Look for Plasmodium parasites.
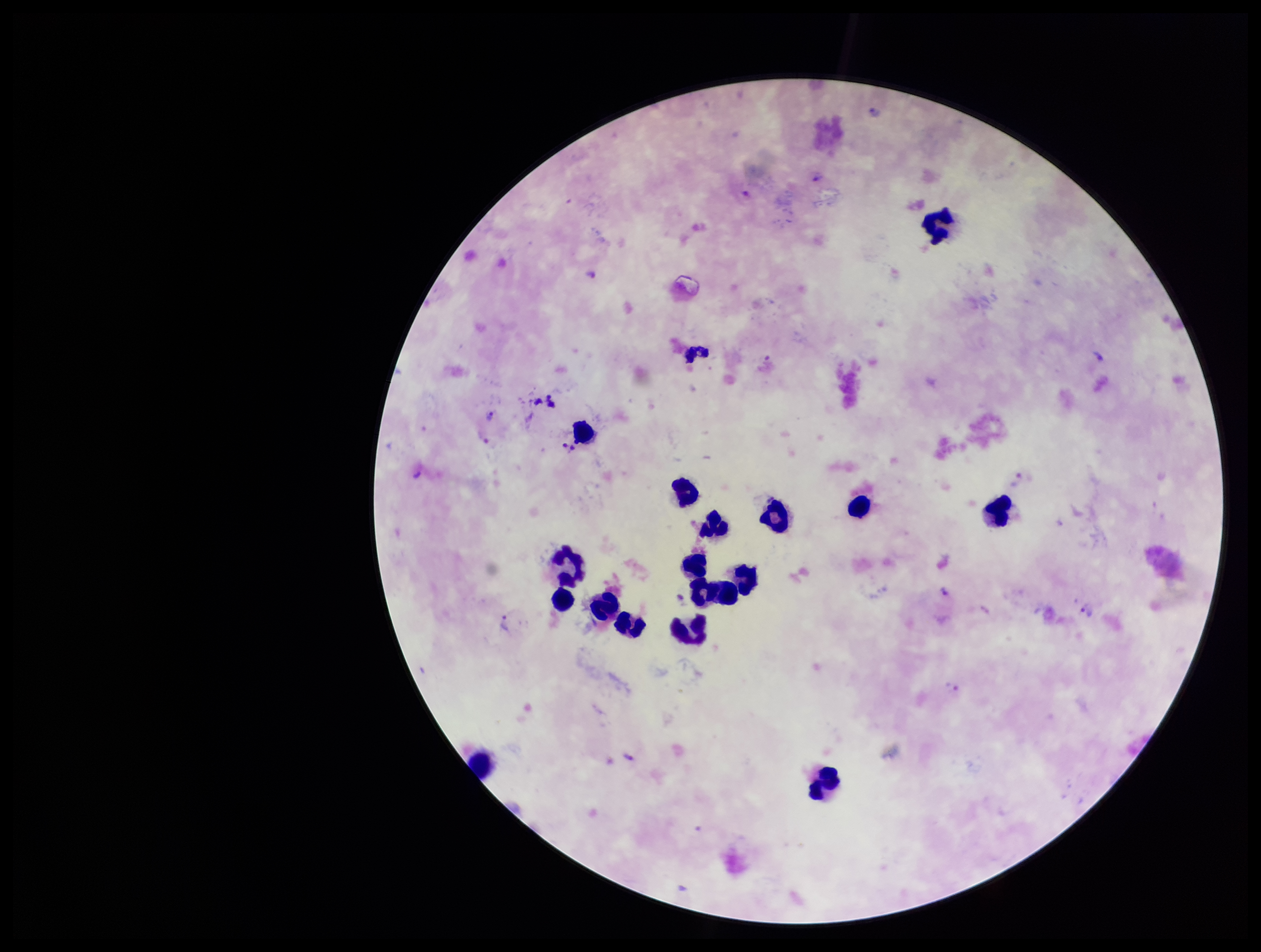

Identified.

field of view = one from this slide
stain = Giemsa
capture = smartphone photograph through the microscope eyepiece
image size = 1261×952 pixels
parasite count = 4
patient malaria status = positive
leukocyte count = 17
species reported for this patient = Plasmodium vivax
preparation = thick